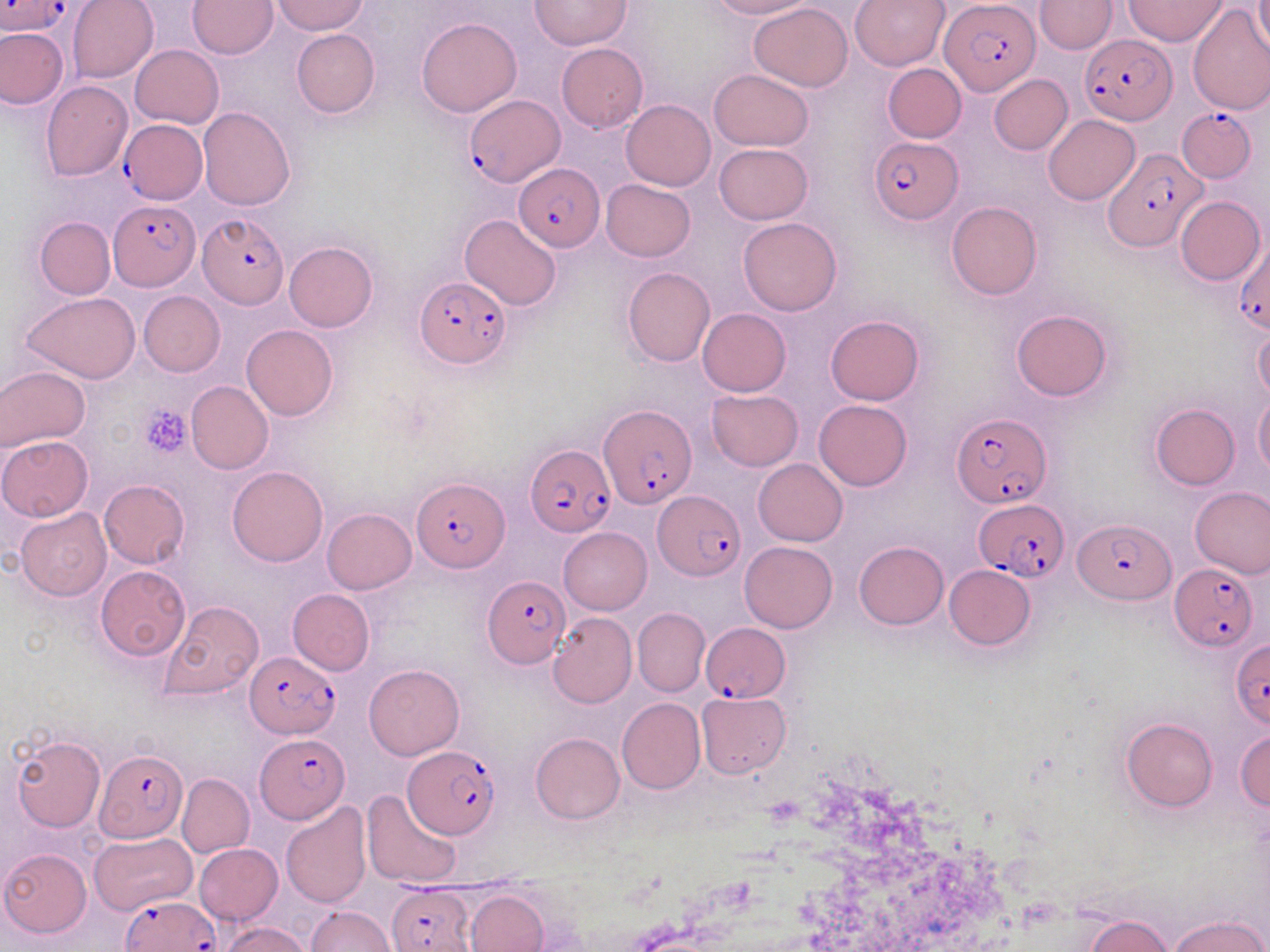

Approximate bounding boxes as (x1,y1)-(x2,y2) corner pairs in pixels. Plasmodium falciparum-infected red blood cell locations (subset): (1,0)-(72,36), (940,0)-(1040,96), (1081,34)-(1174,126), (464,94)-(562,188), (1176,104)-(1257,183), (119,120)-(208,203), (868,135)-(960,223), (1101,148)-(1206,249), (514,164)-(605,251), (108,200)-(200,289), (199,214)-(286,308), (1233,235)-(1270,333), (415,277)-(511,370), (599,404)-(695,509), (951,412)-(1051,509), (525,445)-(613,537), (413,478)-(506,574), (652,490)-(745,581), (973,498)-(1068,581), (1075,518)-(1174,605), (1169,563)-(1258,653), (483,575)-(570,667), (702,621)-(790,703), (1230,640)-(1269,728), (245,650)-(340,736), (254,735)-(348,822), (404,746)-(501,838), (95,750)-(188,843), (387,885)-(475,952), (120,894)-(218,951). Platelet locations: (138,405)-(191,457). Uninfected red blood cell locations (subset): (66,0)-(158,83), (188,0)-(277,58), (272,0)-(368,35), (706,0)-(813,20), (850,0)-(949,72), (1034,0)-(1116,54), (1126,0)-(1227,45), (1255,0)-(1270,60), (532,1)-(630,49), (749,4)-(853,90), (418,17)-(522,117), (0,27)-(67,108), (291,29)-(380,118), (556,43)-(648,132), (130,45)-(224,128), (883,63)-(967,143), (709,69)-(813,151), (989,75)-(1072,155), (42,81)-(133,182), (621,100)-(715,191), (198,107)-(296,211), (1043,115)-(1139,205), (713,143)-(814,225), (601,179)-(695,261), (1176,196)-(1265,285), (945,201)-(1042,300), (461,215)-(562,310), (738,216)-(843,315), (35,217)-(114,299), (284,241)-(378,331), (621,267)-(716,367), (138,291)-(225,376), (22,292)-(141,384), (697,308)-(792,397), (1011,308)-(1113,402), (825,315)-(926,405), (241,325)-(338,421), (1253,327)-(1270,404), (0,367)-(89,452), (186,380)-(272,474), (705,389)-(804,471), (1254,392)-(1270,475), (814,400)-(912,491), (1150,403)-(1240,490), (1,435)-(93,521), (753,459)-(848,546), (227,466)-(327,566), (99,480)-(189,568), (1190,486)-(1270,578), (15,507)-(111,600), (322,508)-(416,595), (560,526)-(652,614), (739,540)-(838,633), (854,541)-(948,629), (944,564)-(1035,651), (95,566)-(190,661), (158,600)-(265,699), (633,608)-(709,696), (548,612)-(636,708), (364,664)-(464,759), (695,691)-(791,777), (617,698)-(705,795), (1123,718)-(1218,812), (1234,729)-(1270,810), (530,732)-(624,824), (11,733)-(106,832), (177,773)-(254,858), (362,789)-(462,889), (280,802)-(371,906), (91,833)-(196,914), (194,844)-(284,926), (1,849)-(91,938), (465,890)-(549,952), (307,905)-(395,952), (1169,915)-(1267,952), (1087,916)-(1173,952), (218,922)-(312,952). Slide-level diagnosis: Plasmodium falciparum. Thin blood film. Image is 1270×952 pixels. May-Grünwald-Giemsa-stained preparation. One field of a larger specimen. Captured at 1000x magnification. Optical microscopy.